Give the extent of all uninfected red blood cells.
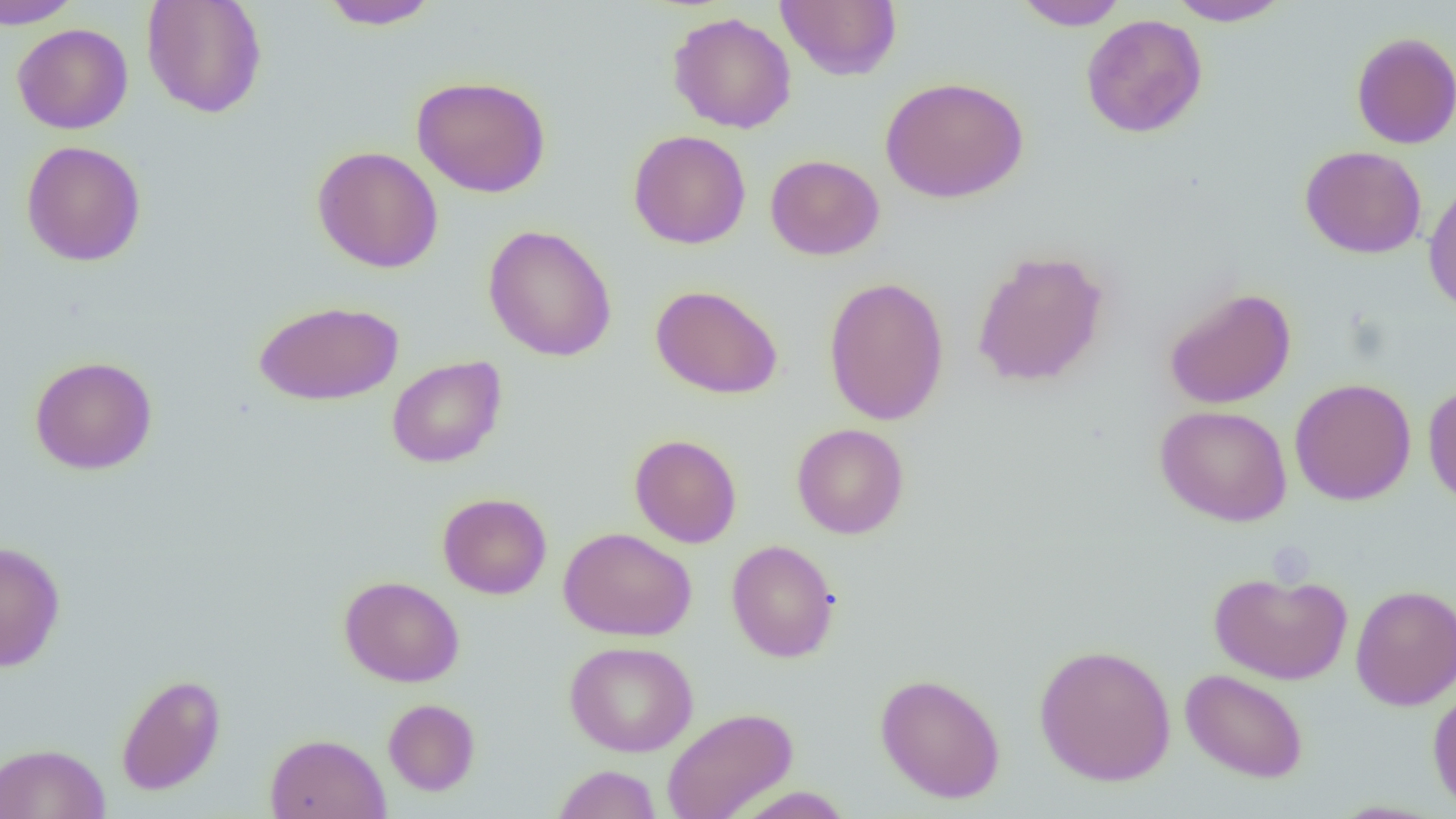
Approximate bounding boxes as (x1, y1, x2, y2) in pixels.
Uninfected red blood cells: (0, 0, 81, 29), (141, 0, 267, 119), (319, 0, 442, 30), (775, 0, 902, 81), (1013, 0, 1130, 30), (1165, 0, 1293, 26), (667, 12, 797, 133), (1080, 14, 1208, 138), (12, 23, 133, 134), (1351, 32, 1456, 149), (411, 75, 551, 197), (880, 76, 1029, 204), (628, 130, 751, 249), (20, 140, 147, 266), (1299, 145, 1427, 259), (312, 146, 443, 273), (765, 154, 884, 260), (1422, 178, 1456, 314), (482, 225, 617, 362), (971, 249, 1110, 388), (823, 276, 950, 426), (650, 284, 783, 399), (1163, 287, 1297, 409), (253, 300, 404, 406), (29, 355, 158, 475), (386, 355, 506, 468), (1289, 378, 1417, 505), (1423, 382, 1456, 508), (1154, 404, 1292, 526), (792, 424, 909, 539), (629, 433, 742, 548), (437, 492, 552, 599), (559, 526, 697, 641), (726, 539, 840, 662), (0, 540, 66, 672), (1209, 570, 1352, 684), (339, 575, 464, 687), (1350, 584, 1456, 710), (565, 641, 698, 757), (1033, 643, 1176, 786), (1179, 668, 1309, 783), (116, 672, 226, 796), (875, 673, 1006, 803), (1427, 681, 1456, 813), (384, 698, 481, 796), (661, 707, 798, 819), (264, 733, 391, 819), (0, 743, 111, 819), (552, 764, 661, 819), (731, 786, 856, 818).

Slide-level diagnosis: no evidence of blood parasites. Light microscopy. 1000x magnification. Image is 1456×819 pixels. One field of a larger specimen. Thin blood smear.